Locate every uninfected red blood cell.
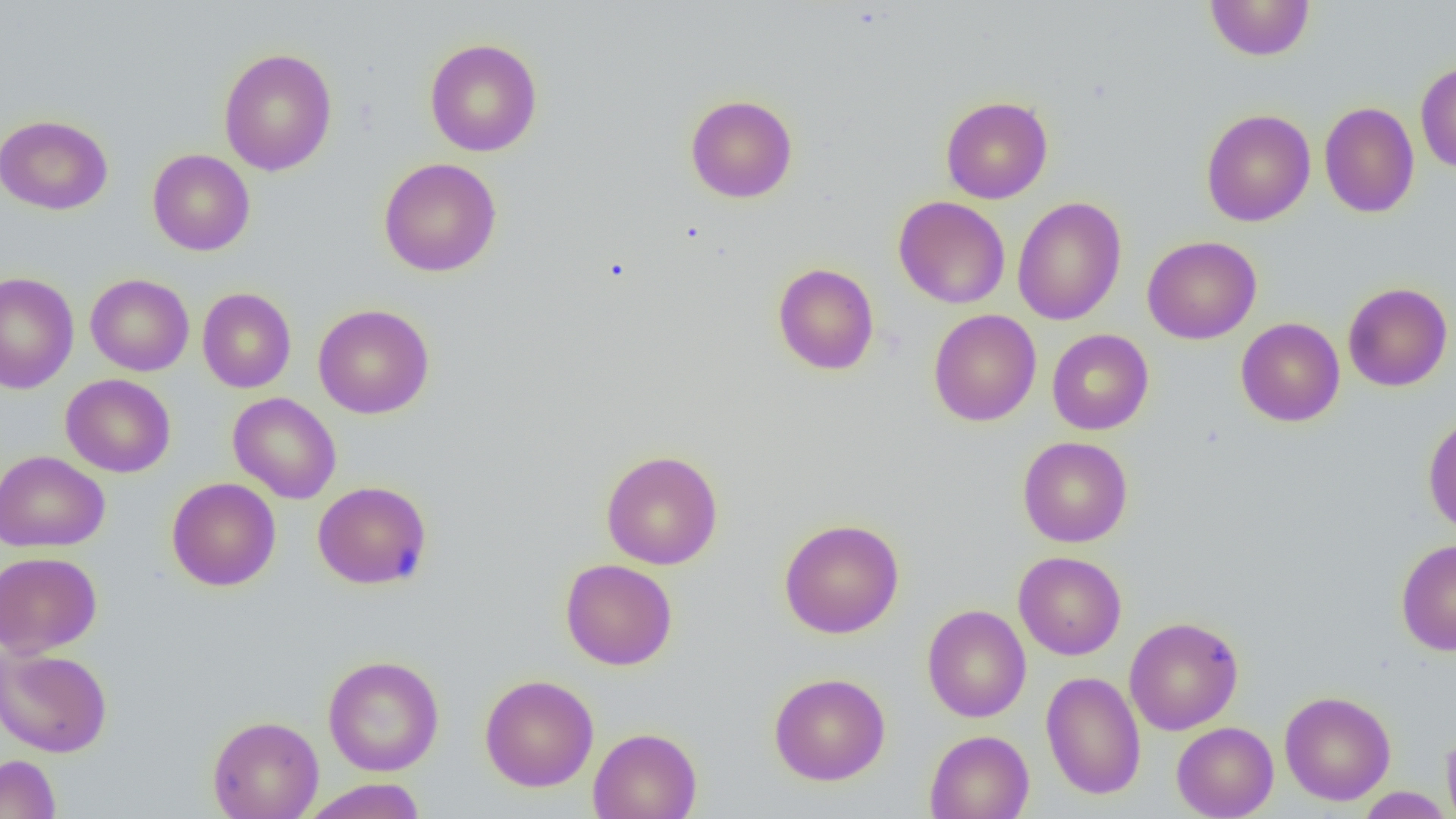
Approximate bounding boxes as [x1, y1, x2, y2] in pixels.
Uninfected red blood cells: [1205, 1, 1314, 61], [424, 38, 543, 157], [218, 47, 338, 176], [1415, 62, 1456, 173], [685, 94, 798, 203], [940, 96, 1053, 204], [1319, 101, 1419, 218], [1201, 109, 1315, 226], [0, 114, 113, 215], [147, 149, 255, 256], [378, 158, 502, 277], [893, 196, 1010, 309], [1012, 196, 1127, 325], [1142, 236, 1261, 344], [772, 263, 879, 375], [0, 272, 79, 394], [85, 273, 194, 376], [75, 274, 181, 476], [1343, 282, 1453, 392], [197, 287, 296, 393], [313, 303, 435, 419], [928, 309, 1041, 426], [1236, 318, 1345, 426], [1047, 329, 1154, 435], [61, 373, 175, 477], [228, 392, 342, 504], [1422, 413, 1456, 537], [1018, 436, 1133, 547], [600, 449, 723, 570], [0, 450, 110, 552], [167, 477, 281, 591], [312, 480, 432, 589], [778, 518, 905, 639], [1396, 538, 1456, 655], [0, 551, 102, 658], [1014, 551, 1127, 660], [559, 558, 677, 670], [922, 604, 1031, 722], [1124, 616, 1243, 735], [0, 645, 113, 757], [323, 655, 444, 777], [1041, 671, 1146, 799], [768, 672, 891, 786], [480, 674, 599, 792], [1280, 690, 1396, 805], [1172, 710, 1396, 810], [207, 714, 324, 819], [1171, 721, 1278, 819], [1442, 726, 1456, 819], [588, 727, 702, 819], [924, 729, 1034, 819], [0, 754, 61, 819], [300, 778, 427, 819], [1354, 787, 1453, 818].

Slide-level diagnosis: no evidence of blood parasites. Optical microscopy. Captured at 1000x magnification. Image is 1456×819 pixels. One field of a larger specimen. Thin blood film.